State which parasite is depicted.
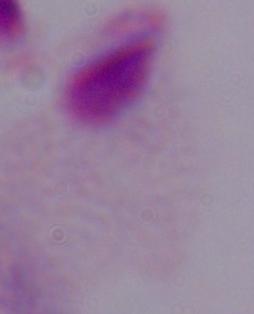
A trichomonad.

modality: photomicrograph
magnification: 1000x